Name the blood parasite species.
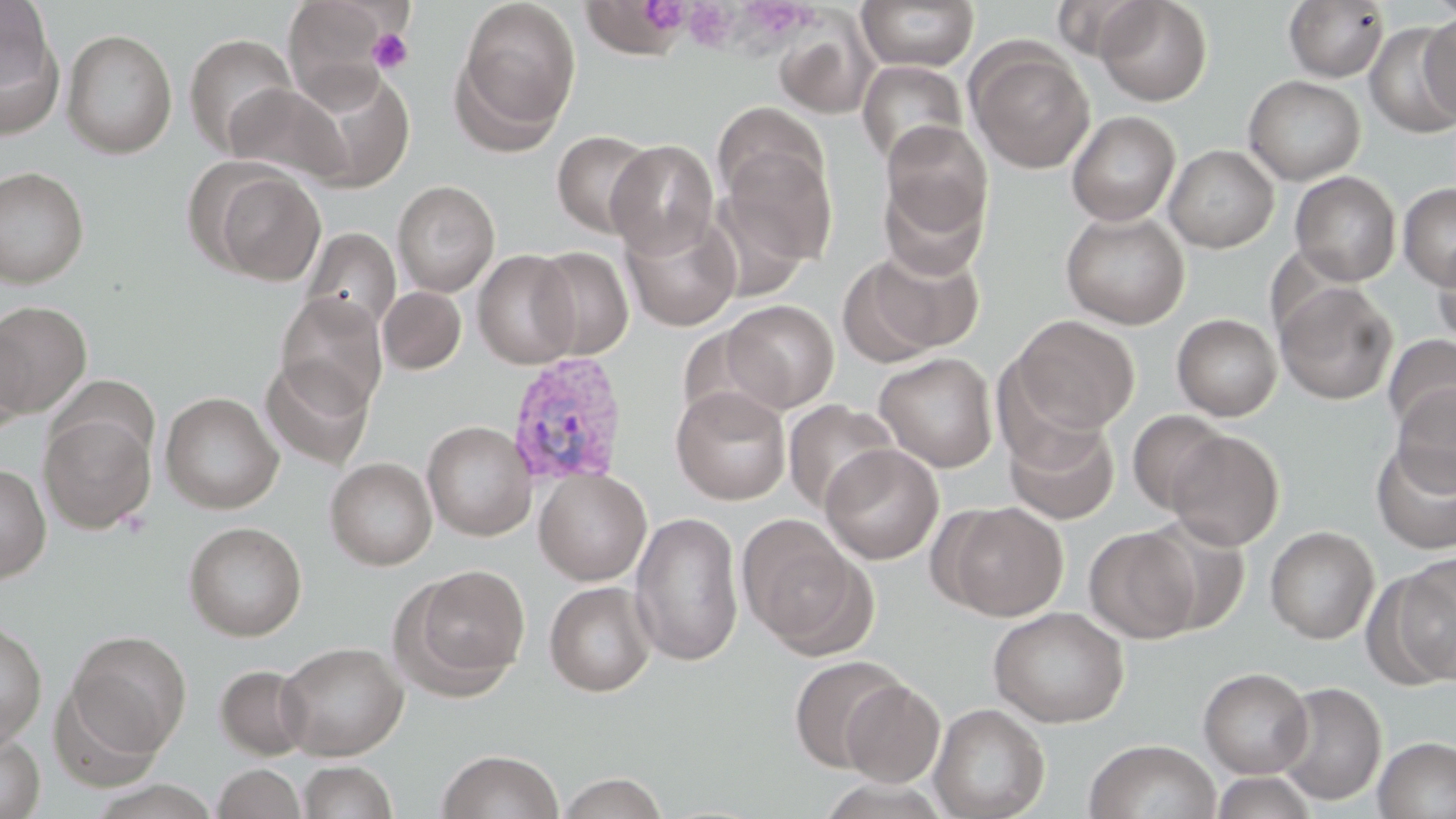

Plasmodium vivax.

preparation: thin blood film
image_size: 1456×819 pixels
platelet_locations: 'approximate bounding boxes as (x1,y1)-(x2,y2) corner pairs in pixels: (683,3)-(738,51), (367,28)-(413,75)'
modality: light microscopy
magnification: 1000x
stain: May-Grünwald-Giemsa
field_of_view: one of a larger specimen
uninfected_red_blood_cell_locations: 'approximate bounding boxes as (x1,y1)-(x2,y2) corner pairs in pixels: (282,0)-(401,106), (454,0)-(581,145), (579,0)-(692,60), (856,0)-(979,72), (1095,0)-(1213,105), (0,1)-(63,136), (1283,1)-(1390,83), (1419,11)-(1456,125), (774,15)-(877,120), (1365,23)-(1455,138), (62,28)-(177,159), (184,33)-(298,156), (967,43)-(1095,174), (856,60)-(968,169), (288,64)-(415,192), (1243,75)-(1365,185), (222,82)-(351,186), (713,103)-(827,206), (1066,111)-(1181,226), (881,120)-(994,239), (551,129)-(657,238), (606,139)-(719,258), (721,144)-(837,268), (1164,145)-(1279,253), (201,165)-(326,285), (0,166)-(89,288), (1289,171)-(1402,286), (879,176)-(989,280), (392,180)-(500,297), (1398,183)-(1456,290), (620,209)-(742,331), (1059,210)-(1190,329), (300,227)-(401,337), (1433,237)-(1456,351), (843,245)-(984,362), (530,246)-(634,360), (472,249)-(581,369), (1274,280)-(1398,406), (379,286)-(466,374), (274,292)-(388,413), (721,299)-(839,413), (0,301)-(92,416), (1171,313)-(1282,421), (1011,315)-(1140,435), (0,324)-(30,438), (1383,334)-(1456,438), (873,352)-(998,473), (260,356)-(375,470), (46,374)-(157,468), (1392,383)-(1456,496), (670,385)-(791,505), (159,391)-(283,514), (782,399)-(899,513), (1127,409)-(1230,514), (39,412)-(156,534), (1004,416)-(1121,525), (422,420)-(536,540), (1165,429)-(1285,550), (1371,441)-(1456,555), (820,443)-(944,565), (325,457)-(437,571), (0,462)-(51,583), (534,468)-(652,586), (936,501)-(1069,621), (629,511)-(744,666), (736,514)-(868,653), (1138,517)-(1253,635), (183,521)-(307,641), (1265,525)-(1379,644), (1083,526)-(1200,643), (1388,553)-(1456,685), (400,564)-(532,694), (544,580)-(657,697), (987,606)-(1129,728), (0,620)-(47,748), (66,630)-(192,757), (276,641)-(409,760), (788,654)-(907,774), (214,664)-(315,761), (1198,666)-(1314,778), (49,677)-(167,790), (840,679)-(945,787), (1273,681)-(1387,806), (928,702)-(1051,819), (0,731)-(45,819), (1373,736)-(1456,819), (1084,740)-(1221,819), (436,748)-(564,819), (296,760)-(399,819), (212,764)-(307,819), (1209,770)-(1321,818), (556,772)-(670,819)'
plasmodium_vivax_infected_red_blood_cell_locations: 'approximate bounding boxes as (x1,y1)-(x2,y2) corner pairs in pixels: (505,353)-(628,488)'